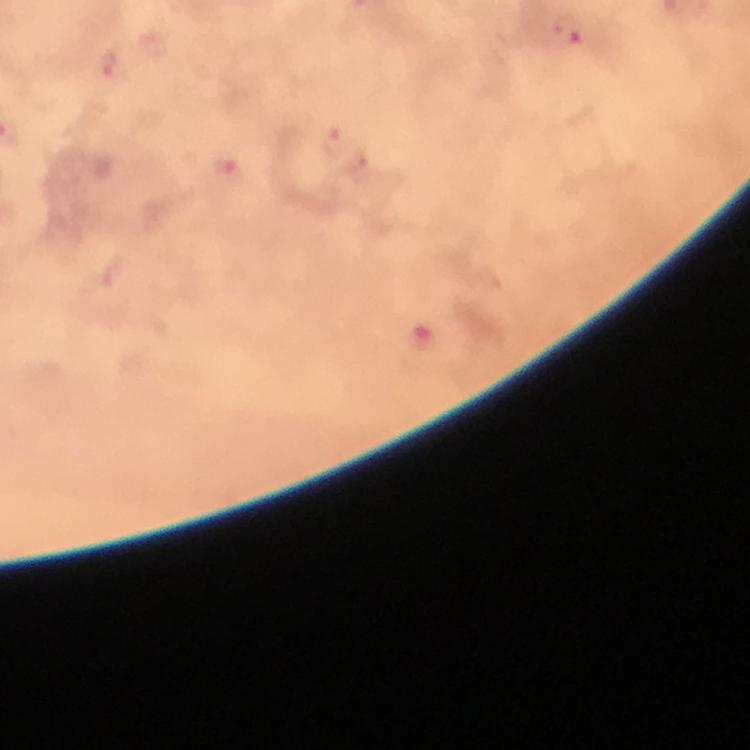
immersion oil = used
capture = smartphone photograph through a microscope
Plasmodium parasite locations = approximate centers as (x, y) in pixels: (565, 33), (112, 66), (336, 139), (227, 168)
stain = Giemsa
preparation = thick blood smear
cropped from = a single field of view
image size = 750×750 pixels
context = from a malaria diagnostic workup
magnification = 100x